Describe the morphology of the red blood cells.
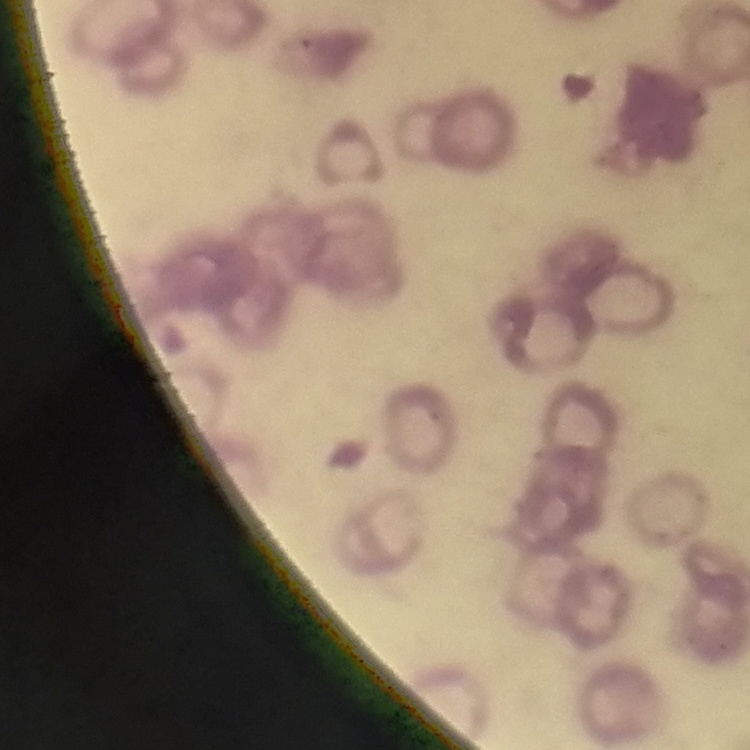
Rouleaux formation.

image type = one tile cut from a larger photomicrograph
preparation = thin blood film
stain = Field's or Giemsa